Name the cell type shown.
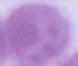
This is an erythrocyte.

Micrograph. 1000x magnification.